State which cell type is depicted.
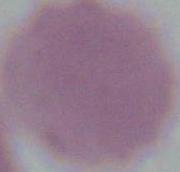

An erythrocyte.

Summary:
  - Magnification: 1000x
  - Modality: photomicrograph